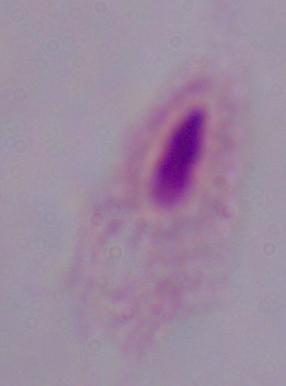 A trichomonad is seen. 1000x magnification. Micrograph.